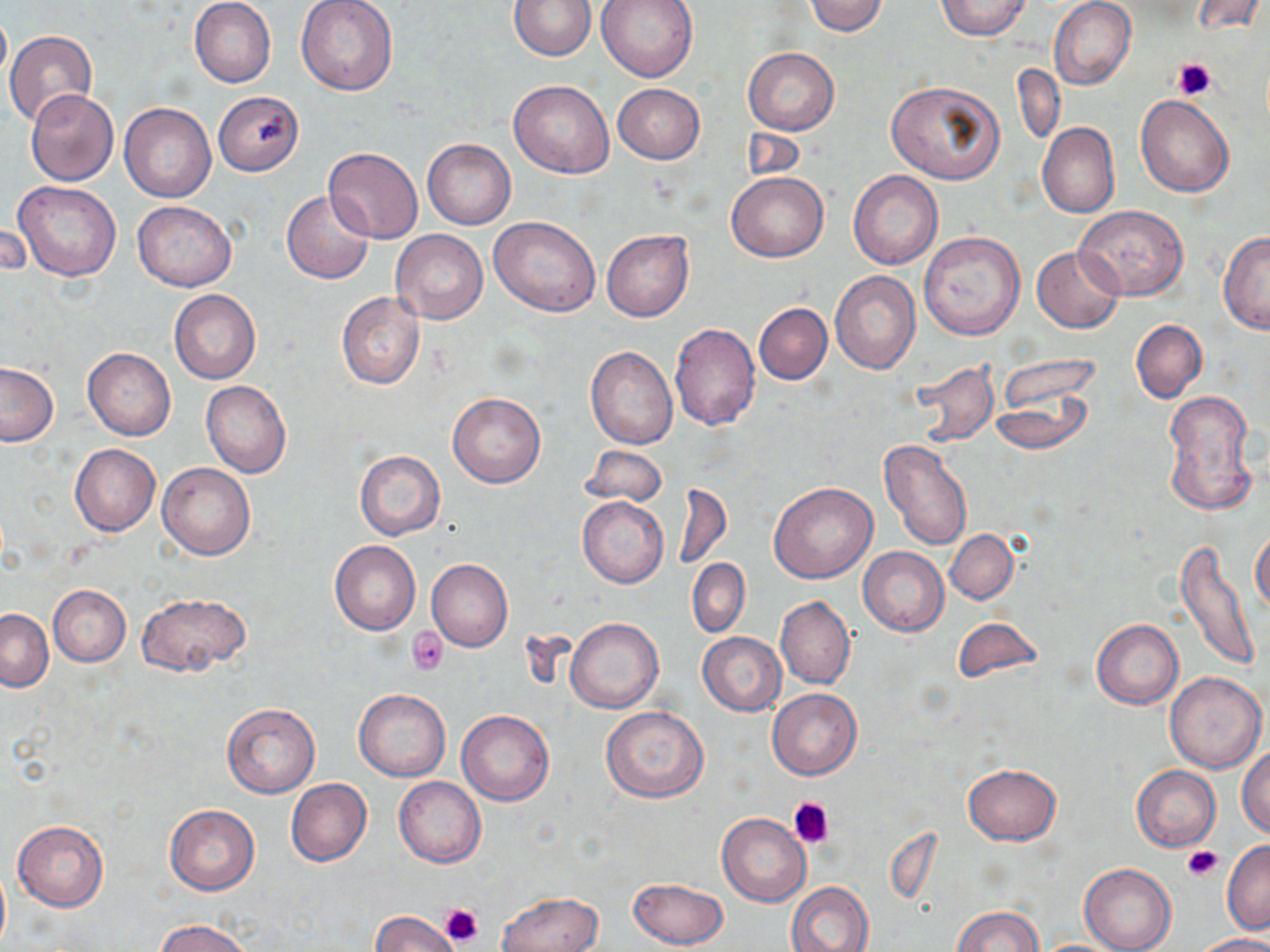
Summary:
  - Coordinate format: approximate bounding boxes as (x1,y1)-(x2,y2) corner pairs in pixels
  - Platelet locations: (1172,57)-(1217,99), (407,627)-(449,674), (789,797)-(836,848), (1182,845)-(1224,882), (440,903)-(484,949)
  - Uninfected red blood cell locations: (189,0)-(276,88), (296,0)-(398,96), (510,0)-(596,60), (596,0)-(698,82), (1049,0)-(1135,90), (1189,0)-(1265,35), (802,1)-(889,36), (936,1)-(1030,40), (0,8)-(10,90), (4,30)-(98,128), (742,48)-(838,135), (1012,64)-(1065,145), (887,79)-(1005,184), (509,81)-(614,178), (613,84)-(705,163), (25,89)-(118,186), (213,91)-(303,176), (1135,95)-(1234,197), (118,103)-(216,202), (1036,122)-(1120,218), (741,126)-(806,180), (422,138)-(517,229), (324,147)-(424,243), (848,170)-(943,269), (727,172)-(827,262), (13,180)-(121,281), (282,190)-(373,284), (131,200)-(237,291), (1076,205)-(1188,299), (489,216)-(601,317), (2,219)-(30,281), (390,229)-(488,324), (602,230)-(693,322), (919,231)-(1025,339), (1218,232)-(1269,335), (1032,246)-(1124,333), (830,270)-(921,373), (169,290)-(261,384), (337,292)-(426,390), (754,303)-(831,385), (1131,320)-(1206,402), (669,323)-(760,430), (586,346)-(677,449), (83,347)-(175,439), (995,356)-(1096,424), (908,360)-(998,446), (0,361)-(58,446), (201,380)-(292,478), (990,388)-(1092,456), (1162,388)-(1258,517), (448,393)-(545,487), (877,440)-(973,552), (70,444)-(160,536), (579,444)-(667,506), (354,449)-(445,540), (158,462)-(255,559), (673,482)-(732,572), (768,484)-(876,584), (577,496)-(667,589), (1251,526)-(1270,616), (945,530)-(1017,603), (1175,538)-(1260,671), (330,540)-(421,635), (858,547)-(949,635), (426,559)-(513,652), (687,559)-(749,637), (48,585)-(131,666), (137,593)-(251,677), (775,596)-(855,690), (1,608)-(53,690), (566,618)-(662,712), (953,619)-(1039,684), (1091,619)-(1183,709), (697,632)-(785,716), (1164,671)-(1266,772), (353,687)-(450,781), (766,688)-(861,781), (222,702)-(320,799), (601,706)-(708,803), (456,710)-(553,805), (1237,746)-(1270,838), (963,764)-(1061,846), (1131,766)-(1221,851), (394,777)-(485,868), (286,779)-(371,866), (165,805)-(260,895), (717,812)-(811,907), (13,820)-(108,911), (1221,840)-(1270,935), (0,860)-(9,952), (1079,863)-(1176,952), (628,877)-(728,949), (787,881)-(873,952), (496,891)-(604,952), (952,906)-(1043,952), (370,911)-(459,952), (157,919)-(251,952), (1190,934)-(1270,952)
  - Slide-level diagnosis: no evidence of blood parasites
  - Modality: light microscopy
  - Preparation: thin blood film
  - Stain: May-Grünwald-Giemsa
  - Magnification: 1000x
  - Field of view: one of a larger specimen
  - Image size: 1270×952 pixels